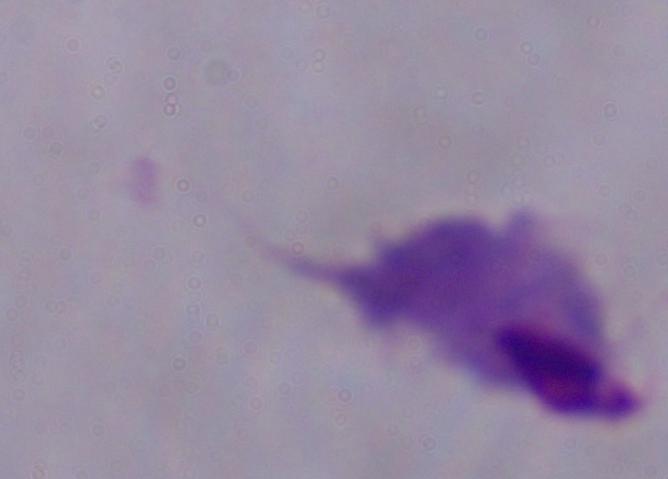

Summary:
  - Magnification: 1000x
  - Modality: photomicrograph
  - Identification: trichomonad